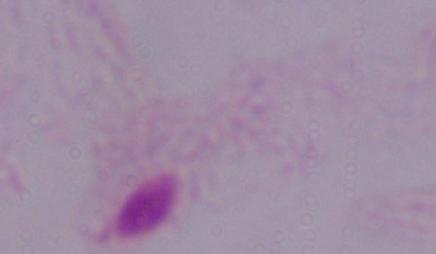

A trichomonad is shown. Micrograph. Captured at 1000x magnification.